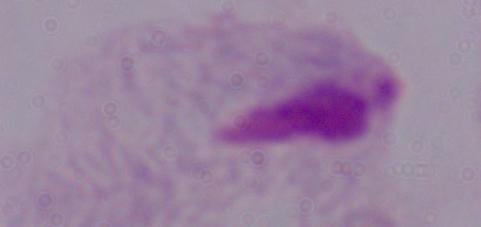

Summary:
  - Modality: photomicrograph
  - Magnification: 1000x
  - Identification: trichomonad